Identify the parasite.
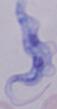

This is a trypanosome.

Photomicrograph. Captured at 1000x magnification.